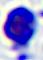

A white blood cell is shown. Captured at 400x magnification. Photomicrograph.